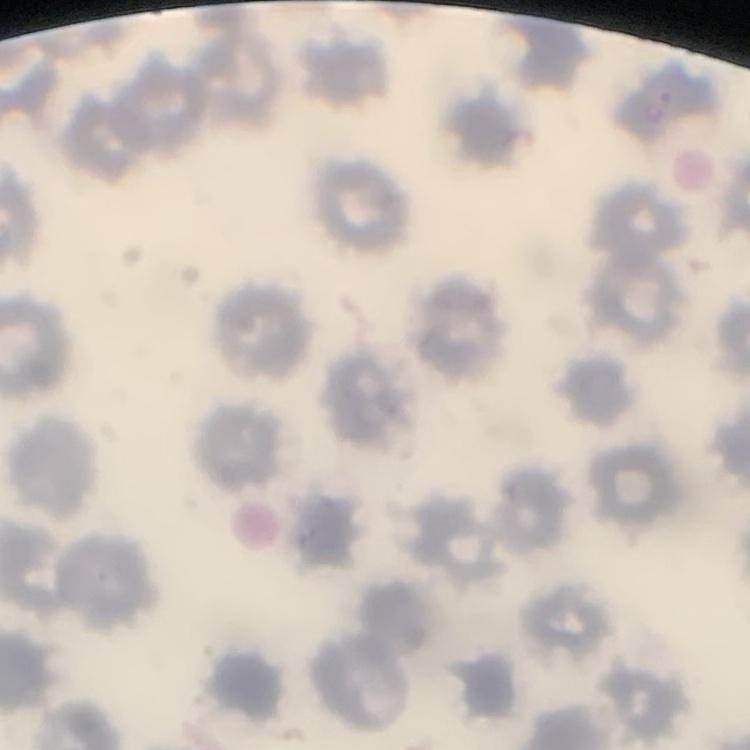
The red blood cells exhibit no rouleaux formation. Stained with either Field's or Giemsa. Thin blood smear. One tile cut from a larger photomicrograph.